Assess the morphology of the erythrocytes.
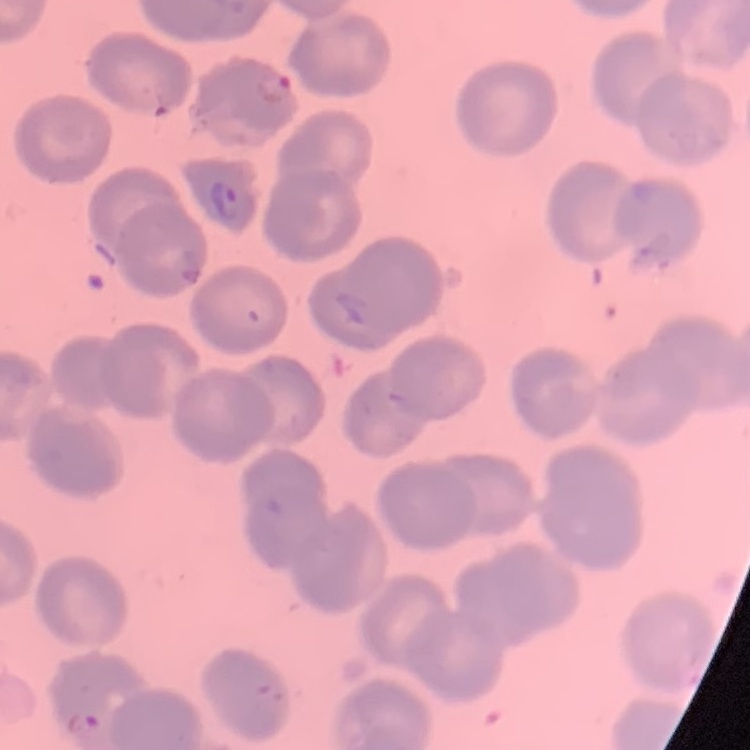
No rouleaux formation.

preparation = thin peripheral smear
image type = one tile cut from a larger photomicrograph
stain = Field's or Giemsa